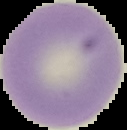
Segmented cell region on a black background. Image is 127×130 pixels. From a thin blood film. Malaria status: uninfected.